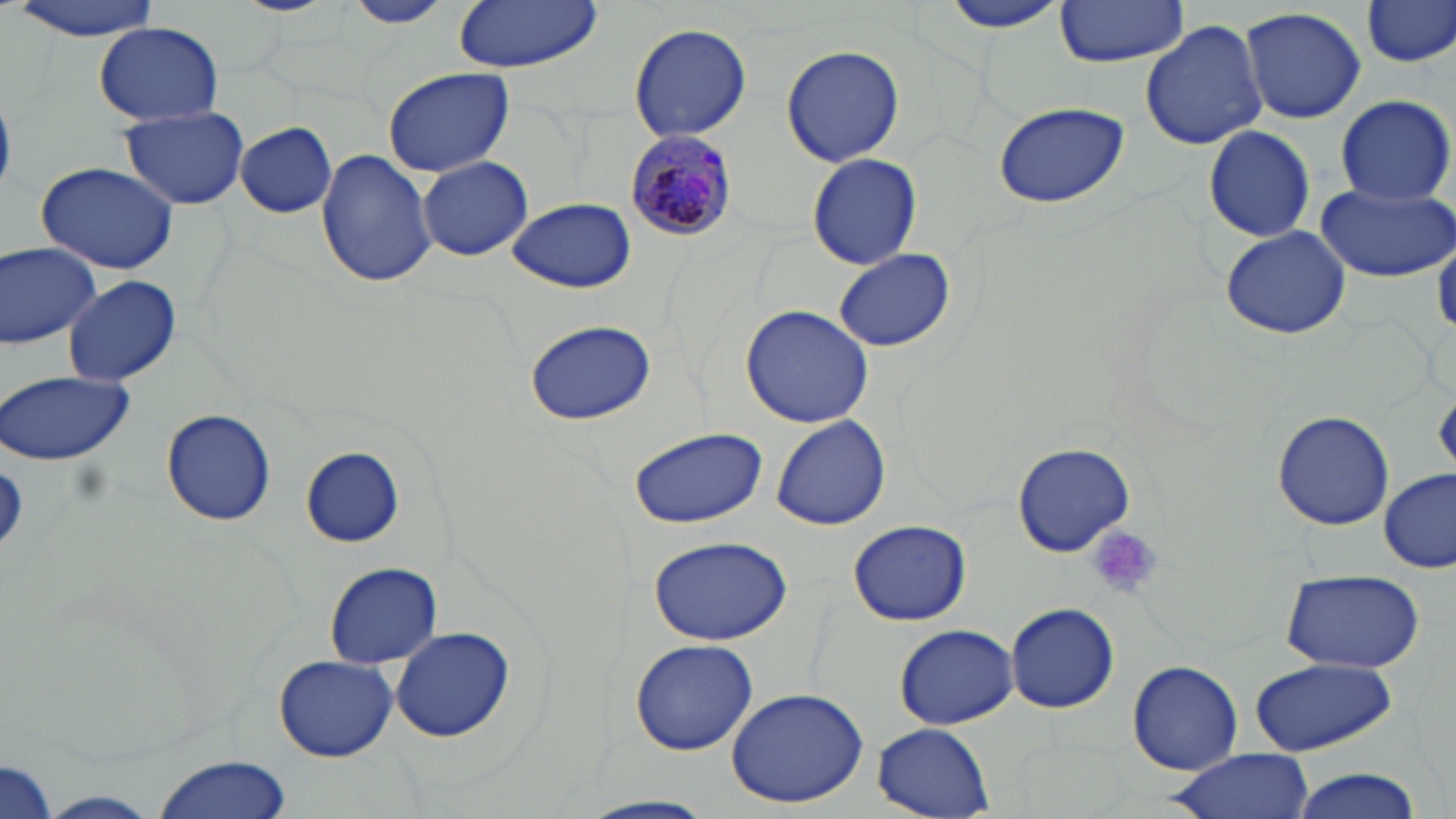

Summary:
  - Coordinate format: approximate bounding boxes as [x1, y1, x2, y2] in pixels
  - Plasmodium malariae-infected red blood cell locations: [624, 131, 736, 243]
  - Platelet locations: [1088, 527, 1161, 600]
  - Uninfected red blood cell locations: [10, 0, 163, 39], [233, 0, 335, 16], [342, 0, 454, 27], [449, 0, 604, 74], [936, 0, 1070, 35], [1053, 1, 1191, 67], [1359, 1, 1456, 69], [1239, 5, 1366, 125], [1140, 20, 1268, 151], [94, 23, 223, 126], [628, 23, 753, 141], [781, 45, 905, 167], [381, 67, 515, 177], [1333, 95, 1454, 205], [991, 101, 1131, 210], [120, 106, 250, 211], [237, 121, 336, 217], [1203, 124, 1317, 242], [316, 149, 437, 287], [807, 153, 920, 270], [417, 155, 533, 261], [37, 161, 180, 275], [1318, 184, 1455, 282], [506, 197, 640, 293], [1219, 226, 1351, 340], [1434, 234, 1456, 338], [0, 242, 101, 349], [834, 250, 954, 351], [61, 274, 182, 386], [739, 304, 875, 429], [523, 320, 657, 426], [0, 370, 135, 467], [162, 409, 276, 527], [1272, 410, 1394, 531], [771, 414, 890, 530], [627, 427, 766, 530], [1012, 442, 1134, 556], [300, 447, 404, 546], [1379, 470, 1454, 574], [847, 519, 972, 626], [642, 535, 793, 644], [323, 560, 444, 668], [1280, 568, 1425, 673], [1005, 602, 1119, 713], [894, 624, 1017, 728], [390, 626, 517, 743], [629, 640, 759, 756], [273, 655, 398, 763], [1249, 658, 1398, 757], [1128, 661, 1243, 775], [724, 685, 872, 809], [873, 724, 994, 816], [1164, 750, 1316, 819], [149, 754, 294, 819], [0, 757, 59, 819], [1287, 769, 1426, 819], [41, 791, 161, 817], [576, 796, 722, 819]
  - Slide-level diagnosis: Plasmodium malariae
  - Stain: May-Grünwald-Giemsa
  - Field of view: single
  - Image size: 1456×819 pixels
  - Magnification: 1000x
  - Preparation: thin blood smear
  - Modality: optical microscopy